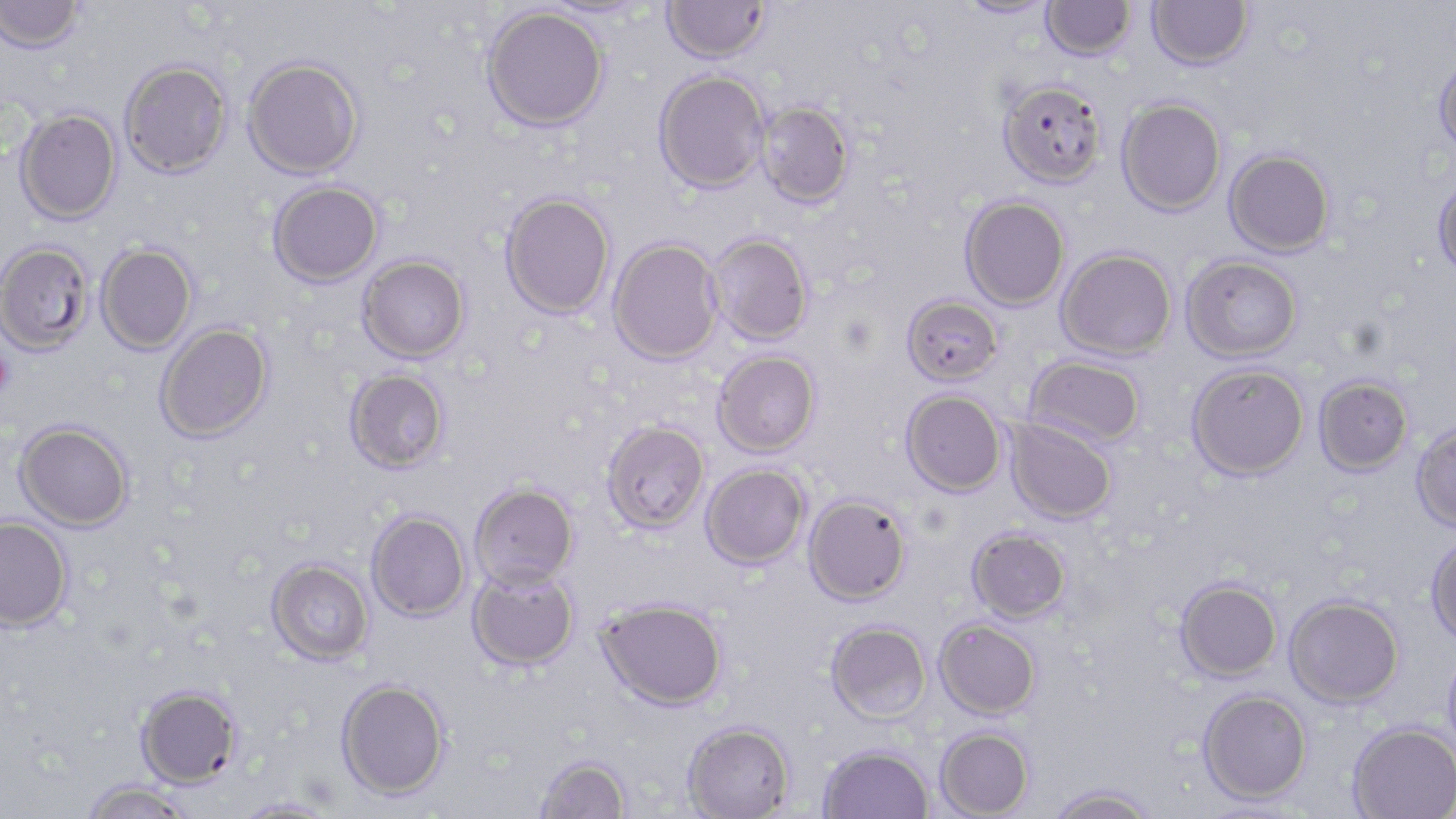

Summary:
  - Coordinate format: approximate bounding boxes as [x1, y1, x2, y2] in pixels
  - Uninfected red blood cell locations: [0, 0, 84, 53], [957, 0, 1057, 20], [1147, 0, 1254, 71], [535, 1, 657, 20], [662, 1, 770, 63], [1040, 1, 1136, 60], [482, 6, 608, 132], [1433, 53, 1456, 161], [242, 57, 363, 179], [119, 60, 233, 178], [654, 70, 769, 193], [998, 79, 1107, 188], [1116, 97, 1227, 216], [756, 101, 854, 208], [15, 108, 121, 224], [1223, 148, 1335, 257], [1432, 172, 1456, 281], [268, 180, 383, 287], [500, 192, 615, 319], [960, 195, 1070, 310], [707, 233, 813, 344], [608, 237, 723, 365], [0, 241, 94, 356], [96, 243, 197, 354], [1056, 247, 1177, 361], [357, 255, 470, 362], [1181, 255, 1301, 363], [901, 295, 1003, 386], [155, 322, 273, 442], [713, 349, 820, 456], [1024, 356, 1146, 448], [1186, 363, 1309, 480], [345, 368, 449, 473], [1314, 375, 1413, 476], [901, 390, 1007, 496], [1005, 418, 1117, 525], [602, 420, 709, 533], [15, 421, 134, 531], [1411, 423, 1456, 532], [701, 463, 809, 569], [470, 482, 578, 589], [803, 494, 910, 605], [366, 510, 470, 622], [1, 516, 74, 631], [967, 527, 1071, 623], [1426, 533, 1456, 646], [266, 558, 373, 665], [467, 564, 579, 671], [1175, 579, 1282, 683], [1284, 594, 1404, 707], [597, 598, 727, 710], [934, 618, 1042, 719], [825, 620, 932, 723], [1442, 646, 1456, 763], [336, 679, 449, 799], [136, 685, 242, 789], [1197, 688, 1312, 804], [683, 722, 794, 819], [1347, 722, 1456, 819], [935, 727, 1035, 818], [819, 744, 934, 819], [535, 755, 631, 818], [82, 780, 194, 818], [1047, 785, 1157, 819], [231, 797, 338, 818], [1195, 800, 1307, 819]
  - Platelet locations: [0, 344, 14, 403]
  - Slide-level diagnosis: Plasmodium falciparum
  - Modality: light microscopy
  - Preparation: thin blood film
  - Stain: May-Grünwald-Giemsa
  - Field of view: single
  - Image size: 1456×819 pixels
  - Magnification: 1000x